State which cell type is depicted.
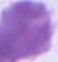
This is an erythrocyte.

Summary:
  - Modality: micrograph
  - Magnification: 1000x